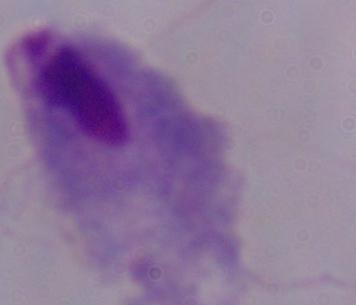
A trichomonad is seen. Micrograph. Captured at 1000x magnification.